Locate every blood parasite and identify its species.
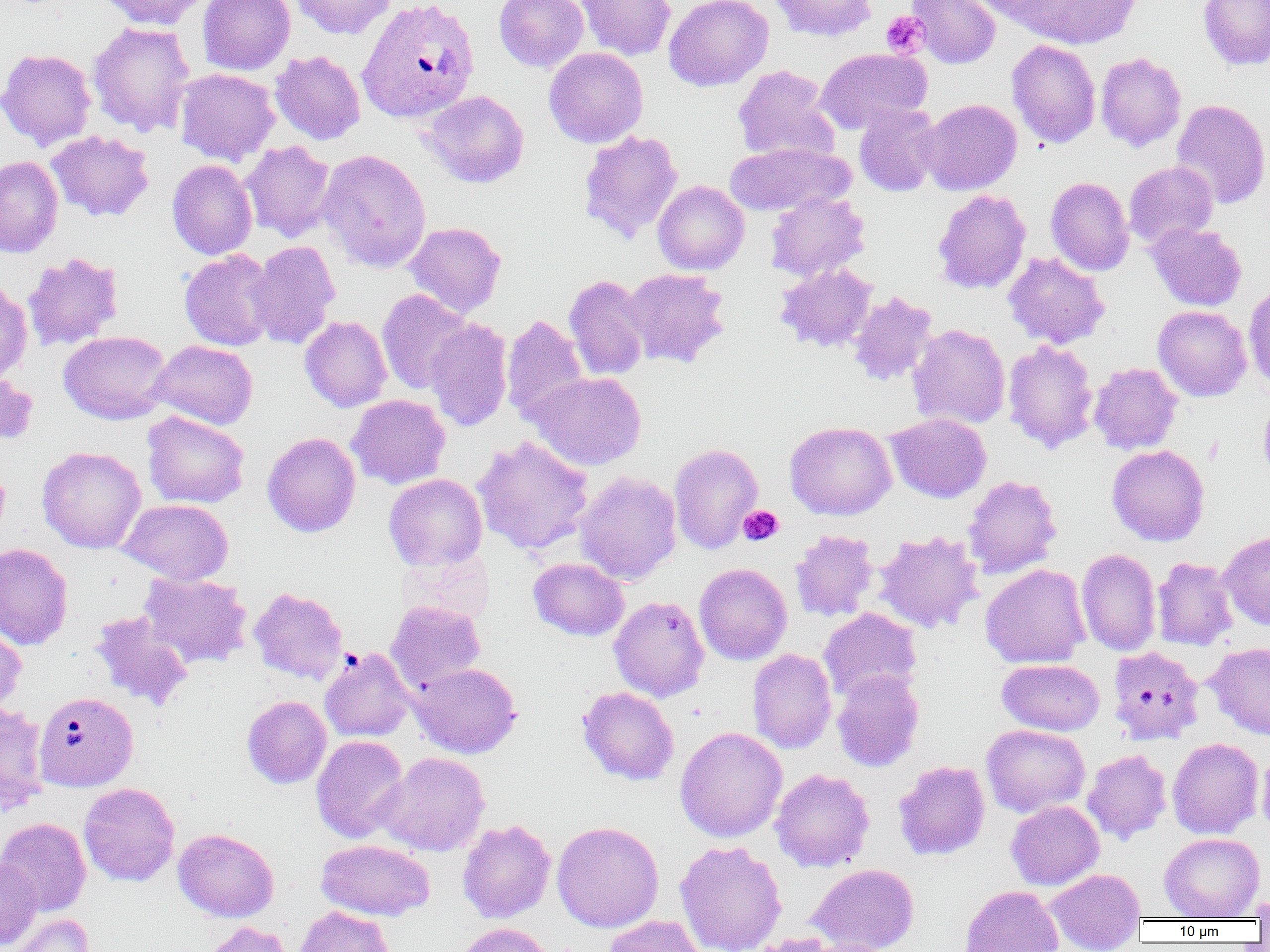

Approximate bounding boxes as [x1, y1, x2, y2] in pixels.
Plasmodium vivax-infected red blood cells: [356, 0, 480, 124], [34, 691, 138, 791].
No Plasmodium falciparum, Plasmodium ovale, Plasmodium malariae, Babesia divergens, or Trypanosoma brucei observed.

{
  "slide_level_diagnosis": "Plasmodium vivax",
  "image_size": "1270×952 pixels",
  "magnification": "1000x",
  "field_of_view": "single",
  "platelet_locations_subset": "approximate bounding boxes as [x1, y1, x2, y2] in pixels: [881, 11, 929, 58], [738, 505, 783, 546]",
  "preparation": "thin blood smear",
  "modality": "optical microscopy",
  "uninfected_red_blood_cell_locations_subset": "approximate bounding boxes as [x1, y1, x2, y2] in pixels: [97, 0, 211, 30], [197, 0, 295, 75], [290, 0, 397, 40], [494, 0, 589, 72], [576, 0, 676, 61], [663, 0, 773, 91], [769, 0, 878, 42], [908, 0, 1001, 69], [1007, 0, 1144, 49], [1197, 0, 1270, 70], [87, 22, 195, 138], [1007, 39, 1101, 148], [544, 47, 648, 148], [815, 47, 931, 134], [0, 48, 97, 150], [270, 50, 365, 145], [1095, 52, 1186, 153], [733, 65, 839, 163], [175, 68, 280, 165], [419, 90, 530, 188], [918, 99, 1022, 195], [1171, 99, 1270, 210], [854, 104, 942, 197], [45, 130, 155, 222], [578, 130, 683, 243], [241, 141, 336, 242], [725, 142, 853, 216], [318, 149, 432, 273], [0, 156, 63, 257], [167, 159, 257, 260], [1123, 161, 1219, 248], [1046, 176, 1134, 276], [652, 180, 749, 275], [932, 189, 1031, 294], [765, 192, 870, 282], [404, 221, 507, 318], [1146, 222, 1247, 311], [247, 240, 341, 349], [179, 250, 277, 351], [22, 252, 124, 351], [1003, 252, 1109, 349], [775, 263, 878, 353], [621, 268, 730, 368], [564, 274, 649, 381], [0, 280, 32, 384], [1243, 282, 1270, 394], [377, 290, 474, 394], [848, 291, 938, 387], [1153, 305, 1252, 401], [501, 314, 589, 425], [300, 315, 392, 412], [424, 318, 514, 432], [908, 324, 1010, 430], [58, 331, 172, 424], [149, 340, 258, 429], [1002, 340, 1099, 454], [1088, 362, 1183, 454], [527, 371, 647, 471], [1258, 393, 1270, 488], [346, 394, 450, 489], [141, 411, 250, 509], [885, 413, 991, 503], [784, 421, 896, 520], [262, 432, 361, 537], [473, 435, 594, 556], [668, 442, 763, 554], [1106, 444, 1209, 546], [37, 446, 146, 553], [574, 471, 682, 584], [384, 473, 487, 571], [962, 475, 1062, 579], [118, 499, 234, 584], [790, 530, 879, 622], [874, 530, 984, 633], [1218, 530, 1270, 630], [0, 543, 74, 651], [1076, 548, 1161, 656], [528, 557, 629, 641], [1152, 557, 1238, 651], [694, 563, 792, 665], [980, 564, 1091, 668], [139, 572, 252, 669], [249, 587, 348, 684], [609, 595, 709, 702], [386, 600, 486, 692], [818, 608, 922, 703], [89, 611, 195, 712], [0, 622, 26, 715], [1206, 642, 1270, 741], [1107, 646, 1205, 745], [320, 647, 415, 742], [747, 649, 837, 754], [997, 658, 1104, 735], [410, 662, 522, 758], [832, 669, 924, 772], [577, 686, 679, 786], [242, 695, 331, 788], [0, 701, 49, 813], [981, 724, 1090, 817], [675, 726, 787, 842], [311, 735, 410, 843], [1167, 738, 1264, 839], [1257, 745, 1270, 840], [1082, 749, 1172, 845], [376, 751, 490, 856], [893, 760, 990, 860], [769, 768, 875, 872], [78, 782, 180, 886], [1006, 800, 1104, 889], [0, 818, 91, 916], [457, 819, 556, 923], [552, 821, 664, 932], [173, 828, 279, 922], [1159, 832, 1264, 920], [316, 839, 436, 921], [675, 839, 787, 952], [0, 856, 42, 950], [807, 863, 920, 952], [1044, 868, 1145, 951], [959, 885, 1063, 952], [1247, 892, 1270, 922], [293, 905, 395, 952], [8, 913, 93, 952], [603, 915, 706, 952], [202, 921, 295, 952], [455, 922, 558, 952], [747, 932, 849, 952], [779, 937, 896, 952]"
}